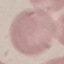
Malaria status: uninfected. Thin smear of blood. Giemsa stain. Acquired by smartphone through the microscope eyepiece. Automatically extracted cell patch, resized to 64 × 64 pixels.